Classify this cell by malaria status.
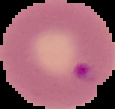

It is parasitized.

image type = segmented cell region with the area outside set to black
preparation = thin blood smear
image size = 115×109 pixels